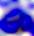

Summary:
  - Magnification: 400x
  - Identification: leukocyte
  - Modality: micrograph